Name the parasite shown.
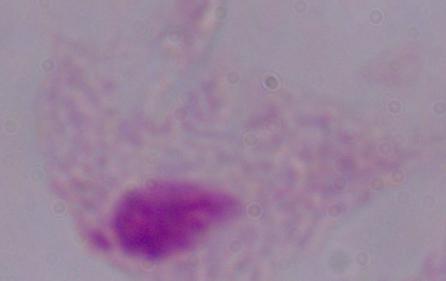
A trichomonad.

Summary:
  - Modality: photomicrograph
  - Magnification: 1000x